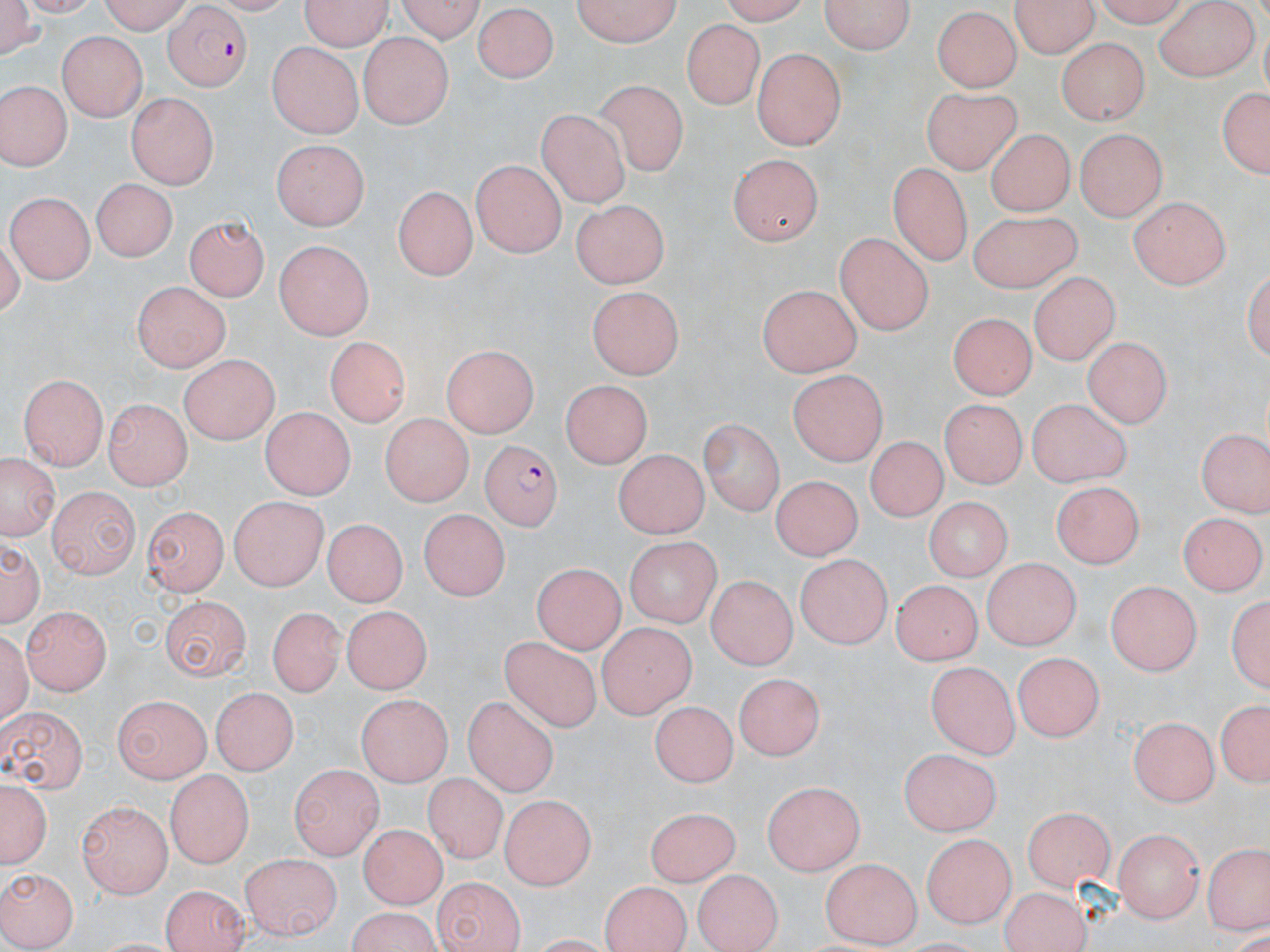
Summary:
  - Coordinate format: approximate bounding boxes as named x1/y1/x2/y2 corners in pixels
  - Uninfected red blood cell locations: (x1=1, y1=0, x2=46, y2=57), (x1=98, y1=0, x2=195, y2=32), (x1=297, y1=0, x2=392, y2=50), (x1=391, y1=0, x2=486, y2=40), (x1=568, y1=0, x2=683, y2=48), (x1=824, y1=0, x2=913, y2=56), (x1=1015, y1=0, x2=1096, y2=60), (x1=1153, y1=3, x2=1261, y2=81), (x1=475, y1=4, x2=556, y2=82), (x1=930, y1=7, x2=1018, y2=92), (x1=680, y1=17, x2=763, y2=109), (x1=55, y1=33, x2=149, y2=120), (x1=356, y1=33, x2=456, y2=126), (x1=1055, y1=35, x2=1152, y2=122), (x1=267, y1=42, x2=365, y2=136), (x1=753, y1=49, x2=848, y2=151), (x1=595, y1=77, x2=689, y2=176), (x1=0, y1=78, x2=72, y2=171), (x1=1214, y1=82, x2=1270, y2=183), (x1=918, y1=86, x2=1024, y2=174), (x1=129, y1=94, x2=215, y2=190), (x1=539, y1=108, x2=627, y2=208), (x1=988, y1=130, x2=1072, y2=219), (x1=1073, y1=131, x2=1165, y2=221), (x1=273, y1=138, x2=373, y2=228), (x1=731, y1=154, x2=820, y2=247), (x1=470, y1=160, x2=563, y2=256), (x1=889, y1=161, x2=971, y2=263), (x1=92, y1=177, x2=176, y2=264), (x1=392, y1=183, x2=474, y2=284), (x1=7, y1=193, x2=95, y2=284), (x1=1126, y1=197, x2=1228, y2=290), (x1=567, y1=198, x2=672, y2=289), (x1=967, y1=209, x2=1079, y2=291), (x1=181, y1=217, x2=268, y2=304), (x1=836, y1=231, x2=934, y2=335), (x1=270, y1=241, x2=373, y2=343), (x1=1027, y1=272, x2=1124, y2=363), (x1=132, y1=278, x2=227, y2=373), (x1=759, y1=286, x2=859, y2=379), (x1=585, y1=288, x2=680, y2=379), (x1=944, y1=317, x2=1033, y2=399), (x1=1085, y1=333, x2=1172, y2=427), (x1=323, y1=338, x2=409, y2=429), (x1=444, y1=347, x2=535, y2=439), (x1=174, y1=356, x2=281, y2=444), (x1=789, y1=370, x2=886, y2=464), (x1=19, y1=373, x2=110, y2=468), (x1=563, y1=382, x2=649, y2=469), (x1=106, y1=397, x2=193, y2=487), (x1=940, y1=397, x2=1030, y2=490), (x1=1028, y1=401, x2=1127, y2=488), (x1=262, y1=406, x2=351, y2=502), (x1=378, y1=415, x2=477, y2=505), (x1=702, y1=421, x2=783, y2=514), (x1=1198, y1=425, x2=1270, y2=515), (x1=863, y1=438, x2=946, y2=524), (x1=613, y1=449, x2=711, y2=536), (x1=3, y1=460, x2=55, y2=541), (x1=772, y1=480, x2=860, y2=563), (x1=1052, y1=482, x2=1145, y2=568), (x1=47, y1=485, x2=141, y2=581), (x1=228, y1=496, x2=329, y2=586), (x1=921, y1=497, x2=1014, y2=580), (x1=143, y1=506, x2=226, y2=597), (x1=418, y1=511, x2=509, y2=602), (x1=1179, y1=511, x2=1263, y2=597), (x1=321, y1=519, x2=405, y2=610), (x1=1, y1=537, x2=44, y2=627), (x1=621, y1=537, x2=720, y2=629), (x1=794, y1=554, x2=891, y2=649), (x1=979, y1=563, x2=1083, y2=650), (x1=529, y1=570, x2=619, y2=653), (x1=707, y1=576, x2=798, y2=668), (x1=890, y1=580, x2=989, y2=665), (x1=1106, y1=580, x2=1200, y2=676), (x1=161, y1=600, x2=249, y2=680), (x1=22, y1=605, x2=112, y2=696), (x1=264, y1=607, x2=347, y2=698), (x1=340, y1=607, x2=433, y2=693), (x1=598, y1=623, x2=694, y2=720), (x1=498, y1=637, x2=606, y2=731), (x1=1010, y1=654, x2=1105, y2=743), (x1=928, y1=661, x2=1017, y2=761), (x1=733, y1=674, x2=826, y2=761), (x1=206, y1=684, x2=297, y2=773), (x1=357, y1=692, x2=451, y2=787), (x1=111, y1=695, x2=208, y2=783), (x1=1213, y1=696, x2=1267, y2=792), (x1=463, y1=698, x2=559, y2=800), (x1=653, y1=700, x2=736, y2=788), (x1=0, y1=706, x2=84, y2=790), (x1=1127, y1=715, x2=1220, y2=803), (x1=899, y1=748, x2=1001, y2=834), (x1=291, y1=765, x2=381, y2=857), (x1=165, y1=769, x2=252, y2=867), (x1=426, y1=774, x2=508, y2=863), (x1=0, y1=776, x2=50, y2=874), (x1=759, y1=778, x2=862, y2=874), (x1=500, y1=795, x2=597, y2=886), (x1=78, y1=800, x2=176, y2=896), (x1=1025, y1=805, x2=1118, y2=885), (x1=644, y1=809, x2=740, y2=884), (x1=360, y1=824, x2=442, y2=909), (x1=1114, y1=829, x2=1203, y2=921), (x1=924, y1=835, x2=1015, y2=927), (x1=1207, y1=840, x2=1266, y2=933), (x1=238, y1=851, x2=341, y2=936), (x1=821, y1=858, x2=922, y2=947), (x1=691, y1=866, x2=782, y2=952), (x1=0, y1=867, x2=74, y2=950), (x1=601, y1=879, x2=692, y2=952), (x1=434, y1=882, x2=522, y2=952), (x1=161, y1=883, x2=248, y2=952), (x1=1001, y1=891, x2=1089, y2=952), (x1=349, y1=911, x2=435, y2=952)
  - Plasmodium falciparum-infected red blood cell locations: (x1=164, y1=9, x2=253, y2=90), (x1=480, y1=441, x2=561, y2=530)
  - Slide-level diagnosis: Plasmodium falciparum
  - Modality: light microscopy
  - Preparation: thin blood smear
  - Magnification: 1000x
  - Stain: May-Grünwald-Giemsa
  - Image size: 1270×952 pixels
  - Field of view: one of a larger specimen